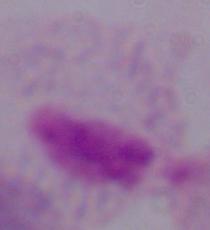
modality: micrograph
magnification: 1000x
identification: trichomonad